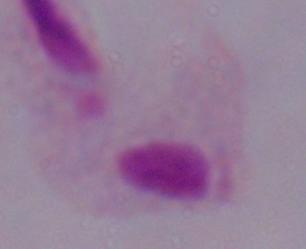

{
  "magnification": "1000x",
  "identification": "trichomonad",
  "modality": "micrograph"
}